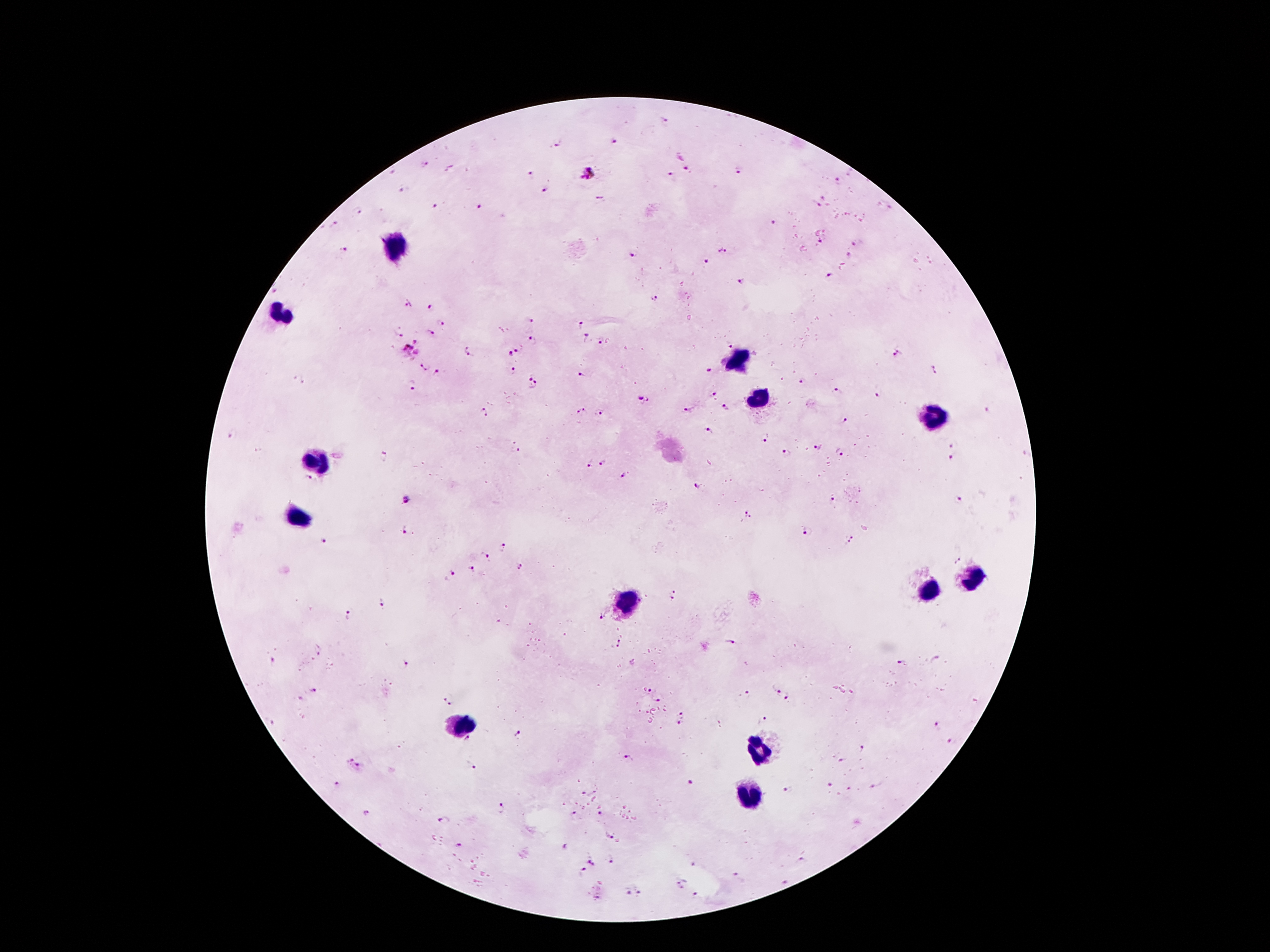
Approximate centers as {x, y} in pixels.
Summary:
  - Plasmodium parasite locations: {666, 120}, {616, 143}, {558, 144}, {422, 161}, {688, 170}, {391, 171}, {738, 171}, {587, 173}, {671, 174}, {530, 175}, {839, 182}, {545, 190}, {403, 191}, {824, 197}, {599, 198}, {817, 203}, {434, 206}, {479, 207}, {360, 209}, {772, 224}, {335, 225}, {820, 241}, {857, 243}, {344, 249}, {722, 251}, {631, 255}, {850, 256}, {706, 263}, {830, 277}, {741, 283}, {275, 290}, {654, 299}, {407, 301}, {430, 307}, {530, 319}, {581, 322}, {442, 323}, {430, 331}, {399, 332}, {586, 338}, {534, 340}, {601, 342}, {729, 344}, {518, 347}, {413, 349}, {470, 352}, {510, 352}, {898, 355}, {424, 365}, {710, 369}, {438, 371}, {514, 371}, {934, 371}, {581, 374}, {298, 378}, {804, 382}, {533, 383}, {412, 384}, {840, 393}, {714, 396}, {878, 396}, {643, 400}, {689, 409}, {725, 409}, {987, 410}, {484, 411}, {581, 411}, {600, 413}, {846, 422}, {708, 433}, {233, 434}, {765, 435}, {952, 444}, {818, 447}, {517, 451}, {786, 453}, {839, 453}, {384, 458}, {951, 458}, {603, 462}, {589, 464}, {622, 476}, {308, 480}, {696, 487}, {407, 499}, {832, 499}, {960, 499}, {749, 515}, {406, 529}, {807, 532}, {324, 542}, {852, 542}, {506, 545}, {487, 554}, {957, 562}, {520, 567}, {472, 569}, {451, 574}, {675, 595}, {384, 601}, {347, 617}, {600, 618}, {620, 643}, {731, 643}, {317, 651}, {273, 663}, {902, 664}, {406, 666}, {651, 689}, {775, 689}, {317, 691}, {746, 696}, {787, 699}, {449, 700}, {658, 700}, {299, 701}, {682, 713}, {269, 721}, {761, 721}, {678, 724}, {718, 724}, {938, 725}, {519, 735}, {466, 740}, {952, 741}, {861, 749}, {627, 759}, {841, 760}, {355, 765}, {473, 768}, {689, 782}, {338, 784}, {830, 784}, {847, 787}, {593, 791}, {788, 791}, {585, 794}, {502, 807}, {367, 813}, {573, 813}, {600, 814}, {444, 821}, {609, 836}, {458, 845}, {563, 847}, {612, 860}, {802, 861}, {592, 863}, {693, 864}, {581, 872}, {738, 876}, {783, 883}, {680, 884}, {639, 891}, {627, 892}, {694, 895}, {598, 897}
  - Leukocyte locations: {394, 241}, {280, 315}, {739, 360}, {757, 397}, {930, 416}, {315, 458}, {297, 515}, {974, 579}, {932, 589}, {631, 602}, {460, 723}, {757, 752}, {749, 797}
  - Magnification: 100x
  - Stain: Giemsa
  - Preparation: thick blood smear
  - Image size: 1270×952 pixels
  - Field of view: one from this slide
  - Patient malaria status: positive for Plasmodium falciparum
  - Capture: smartphone camera through the microscope eyepiece